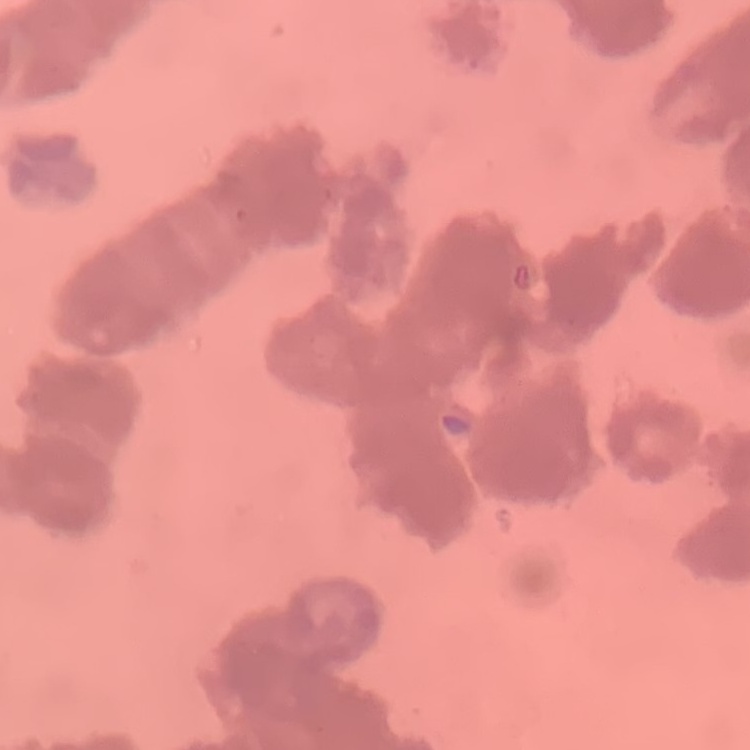

The erythrocytes exhibit rouleaux formation. Square crop of a larger photomicrograph. Stained with either Field's or Giemsa. Thin peripheral smear.